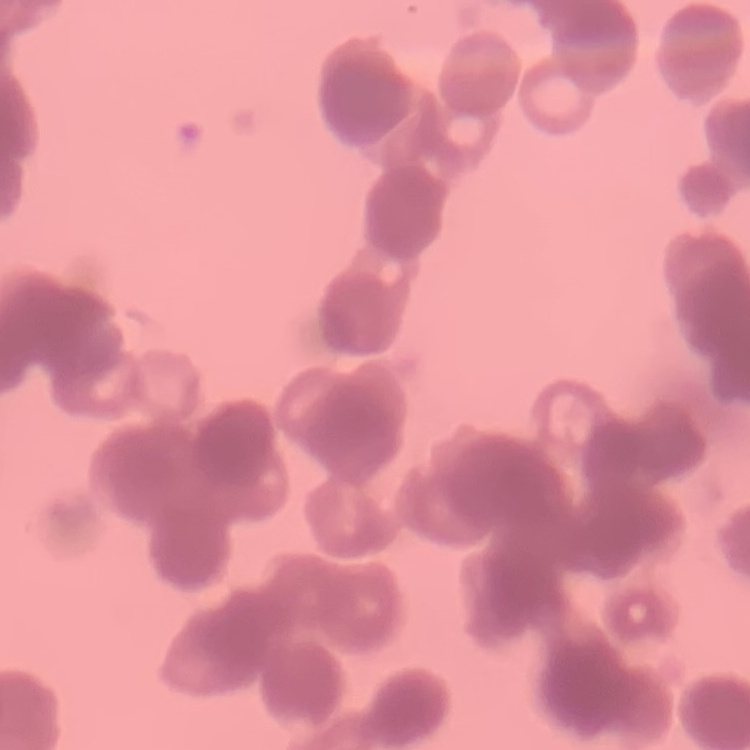
Summary:
  - Red blood cell morphology: rouleaux formation
  - Stain: Field's or Giemsa
  - Preparation: thin blood film
  - Image type: one tile cut from a larger photomicrograph